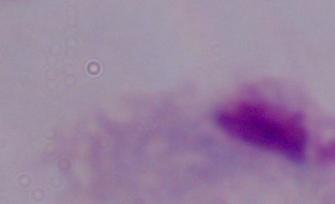
Summary:
  - Modality: photomicrograph
  - Magnification: 1000x
  - Identification: trichomonad